Look for Plasmodium parasites.
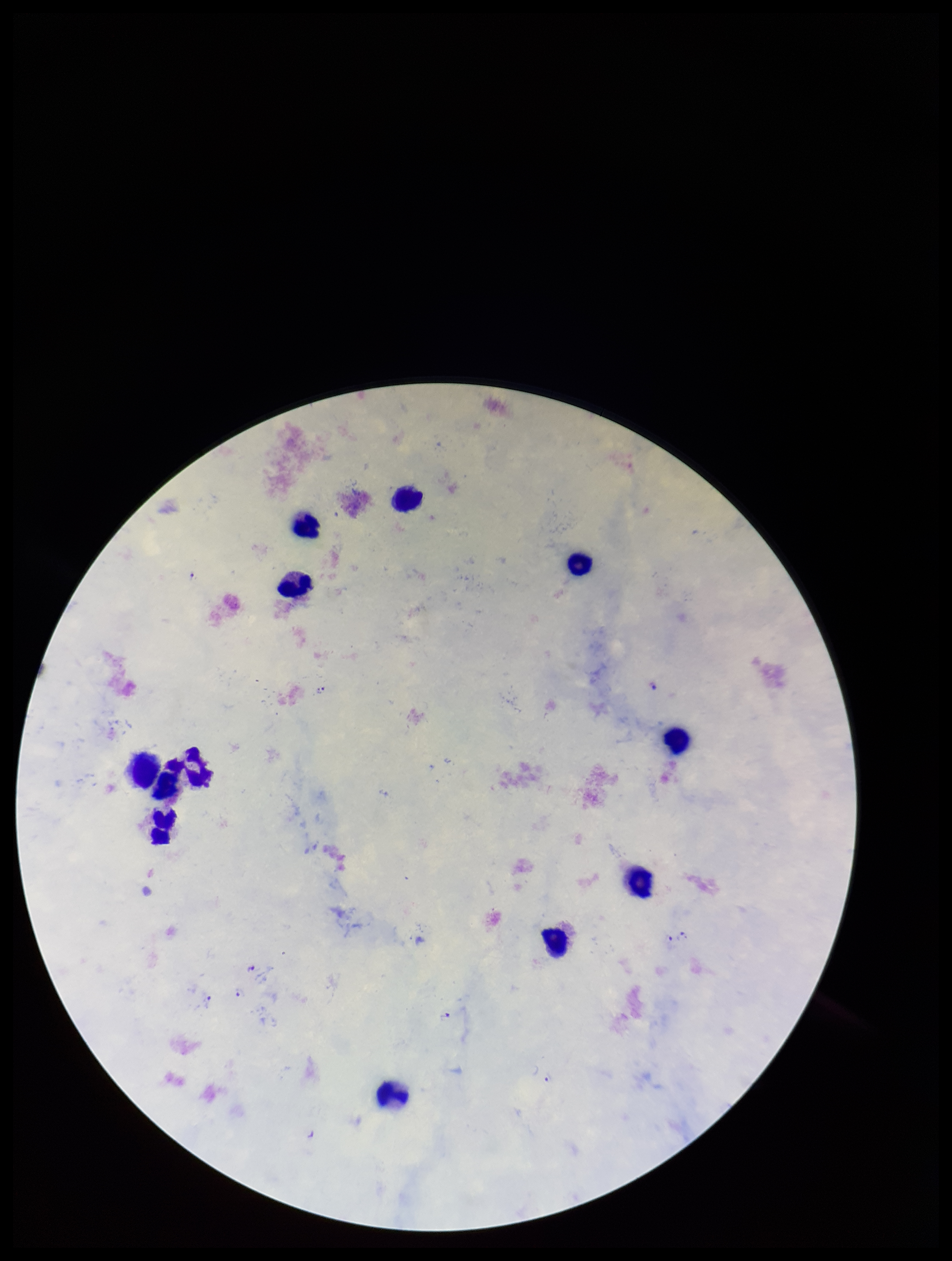
Detected.

Summary:
  - Preparation: thick
  - Capture: smartphone photograph through the microscope eyepiece
  - Image size: 952×1261 pixels
  - Species reported for this patient: Plasmodium falciparum
  - Stain: Giemsa
  - Patient malaria status: positive
  - Parasite count: 11
  - Leukocyte count: 12
  - Field of view: one from this slide